Name the cell type shown.
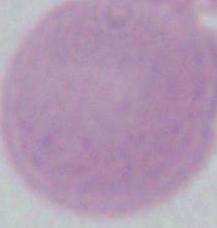

This is an erythrocyte.

magnification = 1000x
modality = micrograph